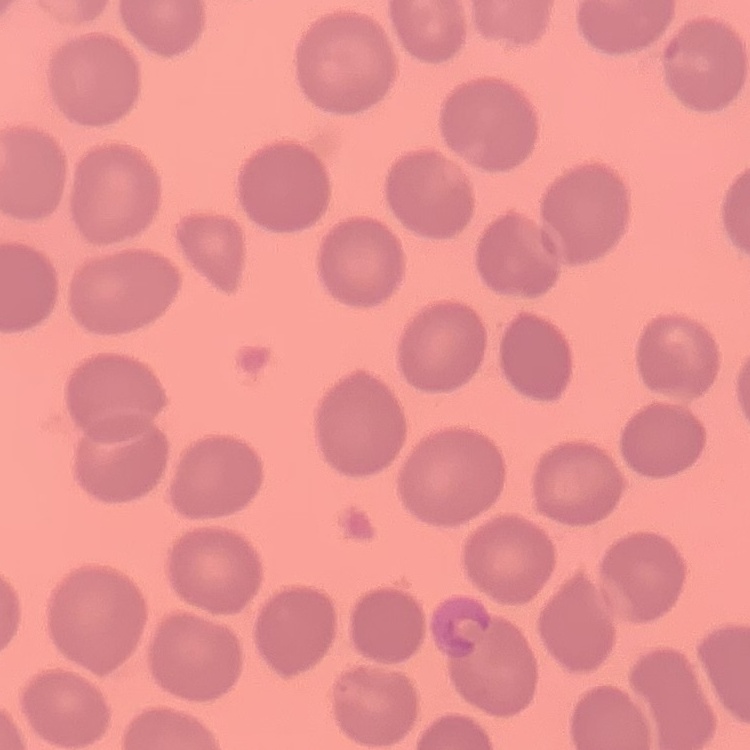

{
  "red_blood_cell_morphology": "no rouleaux formation",
  "stain": "Field's or Giemsa",
  "image_type": "square crop of a larger photomicrograph",
  "preparation": "thin blood film"
}